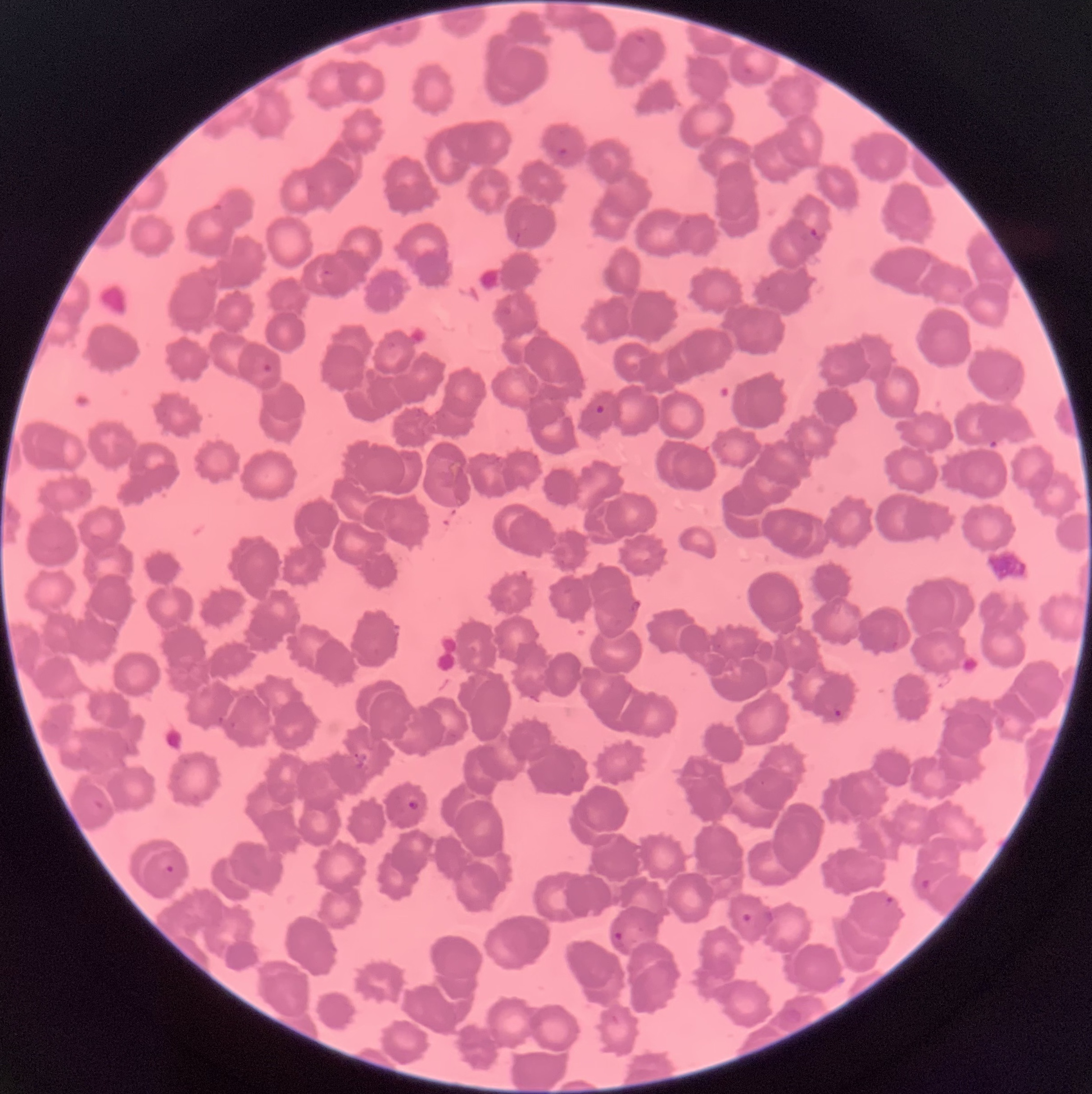

Summary:
  - Coordinate format: approximate bounding boxes as (x1,y1)-(x2,y2) corner pairs in pixels
  - Plasmodium parasite locations: (393,24)-(405,32), (633,33)-(647,46), (743,65)-(756,75), (556,147)-(568,158), (809,227)-(827,241), (322,269)-(333,277), (263,363)-(272,373), (595,404)-(606,415), (833,708)-(843,717), (407,800)-(420,812), (165,864)-(175,874), (920,878)-(937,891), (878,896)-(895,908), (741,911)-(756,923), (611,930)-(627,949)
  - Image size: 1092×1094 pixels
  - Modality: light microscopy
  - Preparation: thin blood smear
  - Red blood cell morphology: rouleaux formation